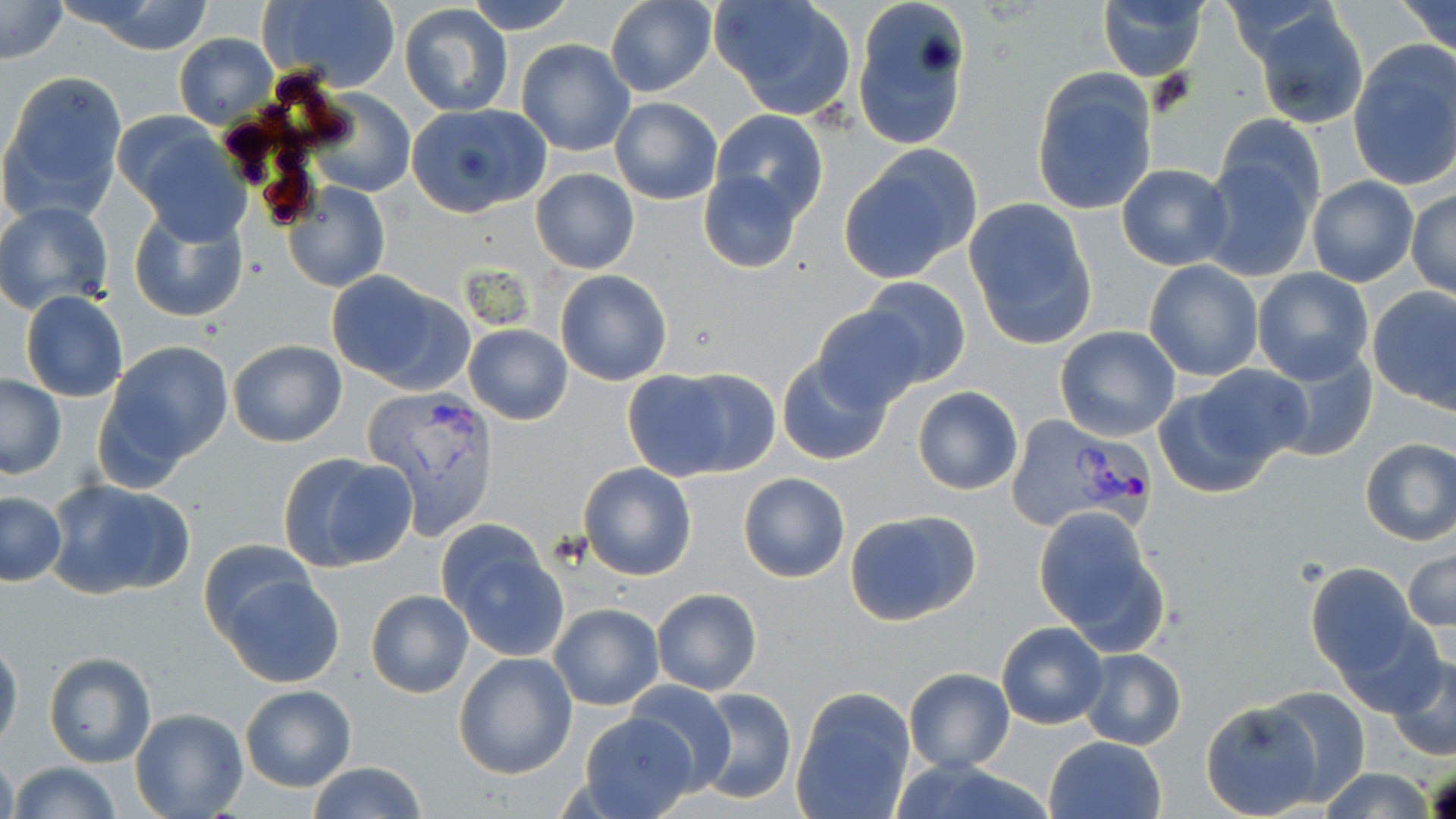

Approximate bounding boxes as [x1, y1, x2, y2] in pixels. Uninfected red blood cell locations: [1, 0, 69, 63], [257, 0, 403, 91], [466, 0, 576, 34], [709, 0, 858, 121], [852, 0, 972, 152], [1397, 0, 1456, 58], [605, 1, 717, 97], [70, 2, 217, 55], [1097, 2, 1208, 81], [399, 3, 513, 117], [1252, 7, 1369, 130], [172, 33, 279, 130], [516, 38, 635, 156], [1349, 40, 1456, 193], [1030, 69, 1159, 215], [1, 72, 128, 222], [309, 91, 415, 196], [609, 98, 723, 204], [404, 102, 551, 219], [709, 109, 829, 227], [1213, 114, 1327, 228], [121, 119, 250, 240], [839, 144, 983, 285], [1198, 150, 1318, 284], [1116, 163, 1233, 270], [698, 167, 805, 275], [531, 168, 639, 273], [1307, 176, 1418, 287], [281, 181, 388, 293], [1408, 188, 1455, 301], [963, 198, 1097, 348], [0, 200, 115, 318], [128, 206, 250, 325], [1143, 259, 1263, 382], [1252, 267, 1374, 384], [326, 270, 473, 394], [554, 270, 672, 386], [858, 276, 972, 388], [1368, 286, 1456, 411], [21, 291, 129, 403], [811, 304, 928, 413], [464, 325, 573, 424], [1054, 327, 1181, 442], [227, 340, 347, 448], [101, 341, 234, 473], [1269, 349, 1378, 463], [777, 357, 890, 465], [621, 366, 772, 481], [1, 373, 66, 478], [1154, 375, 1291, 497], [912, 386, 1023, 495], [1358, 437, 1456, 546], [276, 451, 419, 573], [578, 462, 697, 580], [737, 471, 851, 583], [45, 480, 195, 600], [1, 492, 66, 586], [1032, 505, 1169, 654], [845, 508, 982, 626], [436, 524, 568, 659], [199, 539, 317, 642], [1402, 544, 1455, 637], [1304, 563, 1425, 682], [219, 571, 346, 687], [651, 588, 762, 695], [366, 589, 474, 698], [550, 603, 663, 711], [995, 621, 1107, 729], [0, 638, 23, 752], [1078, 647, 1187, 750], [1387, 651, 1456, 762], [44, 652, 157, 767], [453, 652, 578, 778], [903, 668, 1014, 772], [626, 681, 737, 793], [240, 684, 357, 792], [1262, 685, 1372, 802], [691, 687, 797, 804], [793, 687, 915, 818], [1201, 700, 1326, 818], [131, 708, 249, 818], [580, 712, 700, 819], [1045, 736, 1165, 819], [0, 748, 18, 819], [9, 761, 120, 819], [307, 762, 428, 818], [1319, 766, 1437, 819]. Plasmodium vivax-infected red blood cell locations: [360, 384, 503, 541], [1006, 412, 1159, 534]. Slide-level diagnosis: Plasmodium vivax. May-Grünwald-Giemsa stain. Thin blood film. One field of a larger specimen. Captured at 1000x magnification. Optical microscopy. Image is 1456×819 pixels.